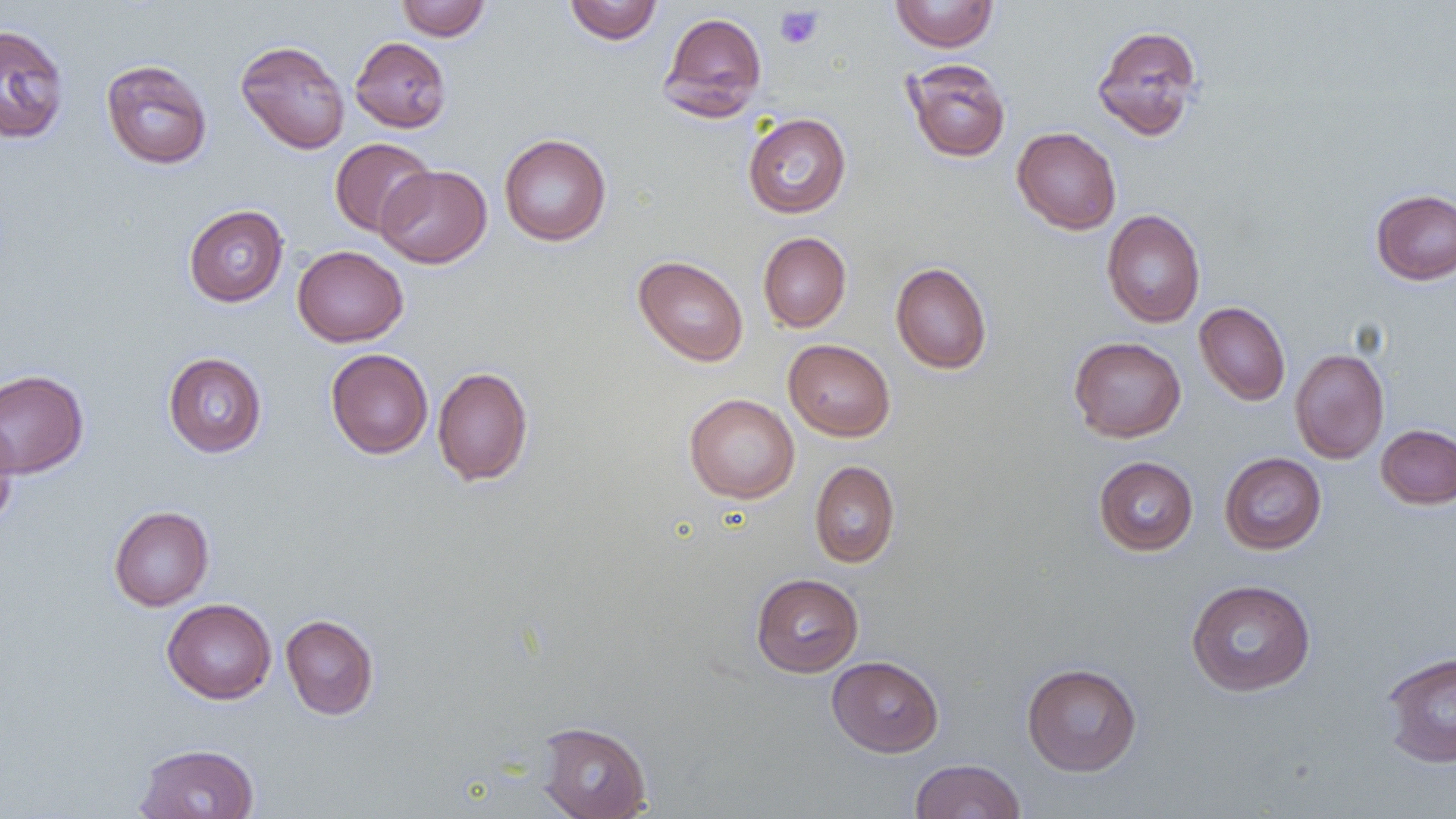 Approximate bounding boxes as (x1,y1)-(x2,y2) corner pairs in pixels. Uninfected red blood cell locations: (396,0)-(491,41), (889,0)-(999,52), (564,1)-(663,45), (659,11)-(767,119), (0,23)-(70,144), (1091,24)-(1203,141), (349,37)-(452,133), (235,39)-(350,154), (903,58)-(1011,163), (100,59)-(213,169), (742,113)-(851,218), (1012,126)-(1122,235), (499,134)-(612,246), (329,138)-(435,237), (376,164)-(492,268), (1370,188)-(1456,285), (183,205)-(289,307), (1102,209)-(1205,328), (758,232)-(852,332), (292,245)-(408,347), (633,255)-(749,367), (890,262)-(992,374), (1194,302)-(1290,406), (1068,336)-(1186,442), (783,339)-(896,441), (326,348)-(433,459), (1290,348)-(1389,464), (163,352)-(267,458), (432,366)-(533,486), (0,369)-(89,479), (684,394)-(800,504), (0,411)-(19,532), (1376,424)-(1456,509), (1219,452)-(1327,554), (1093,456)-(1199,555), (810,460)-(900,568), (109,506)-(214,611), (751,572)-(864,677), (1185,579)-(1316,697), (161,598)-(276,704), (280,614)-(379,720), (1381,651)-(1456,767), (827,655)-(944,757), (1021,662)-(1142,776), (535,721)-(653,819), (134,743)-(260,819), (909,759)-(1026,818). Platelet locations: (775,5)-(823,49). Slide-level diagnosis: negative for blood parasites. Thin blood smear. Captured at 1000x magnification. Optical microscopy. One field of a larger specimen. Image is 1456×819 pixels.